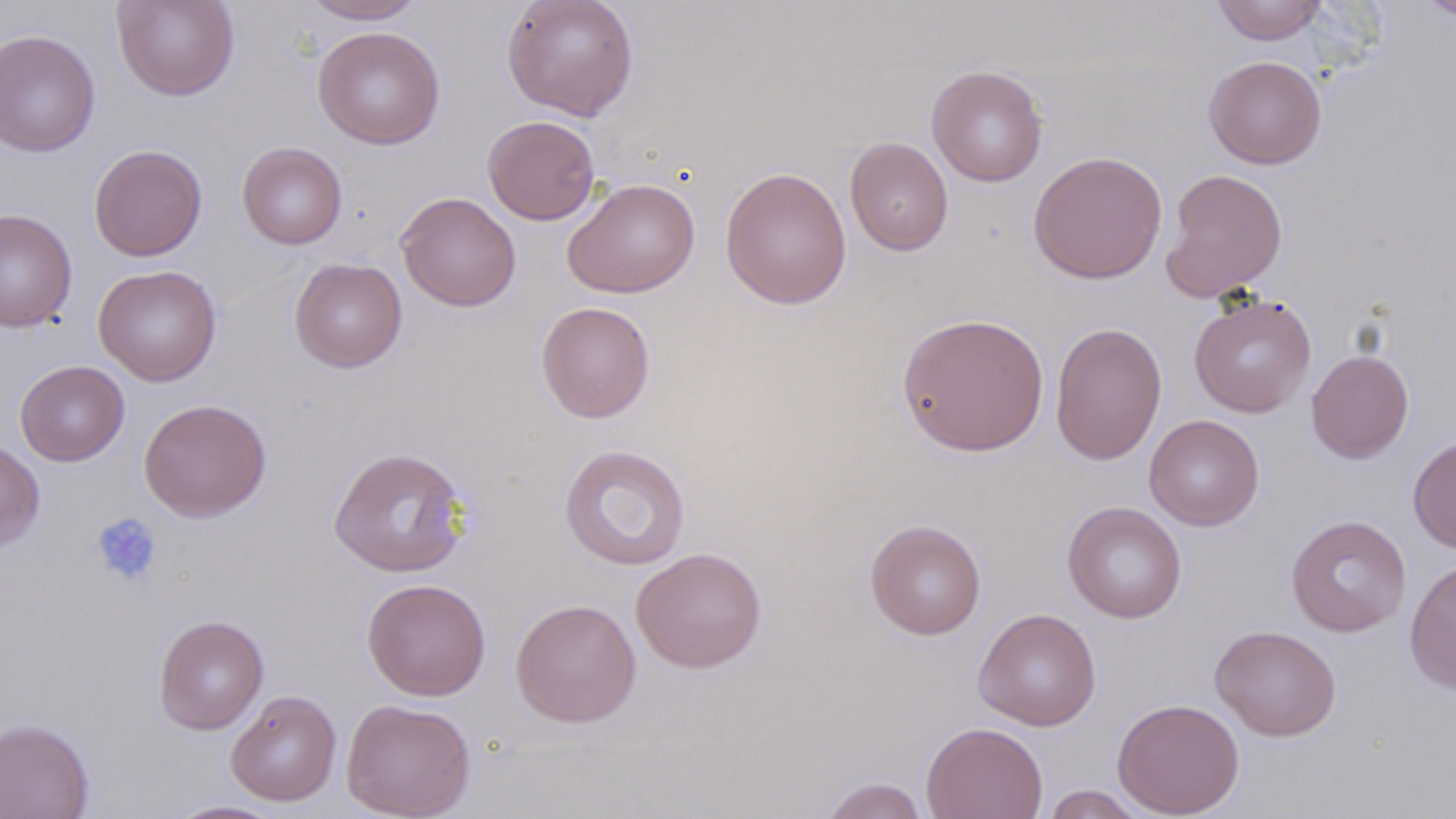

Summary:
  - Coordinate format: approximate bounding boxes as (x1, y1, x2, y2) in pixels
  - Platelet locations: (90, 512, 162, 588)
  - Uninfected red blood cell locations: (111, 0, 240, 101), (300, 0, 427, 24), (502, 0, 639, 121), (1212, 0, 1328, 45), (1418, 0, 1455, 22), (312, 26, 446, 149), (0, 29, 100, 157), (1203, 55, 1327, 169), (927, 65, 1049, 187), (482, 115, 600, 225), (844, 137, 954, 256), (237, 142, 347, 249), (89, 143, 207, 261), (1028, 150, 1168, 285), (720, 166, 852, 310), (1161, 168, 1288, 302), (562, 178, 701, 298), (396, 191, 521, 311), (0, 208, 77, 332), (289, 257, 407, 373), (93, 265, 222, 387), (1189, 293, 1316, 418), (536, 301, 655, 423), (896, 312, 1049, 456), (1049, 321, 1167, 466), (1306, 349, 1414, 464), (15, 360, 130, 466), (138, 398, 272, 522), (1144, 414, 1265, 531), (1408, 435, 1456, 554), (0, 438, 45, 551), (558, 444, 691, 571), (328, 446, 471, 578), (1062, 502, 1187, 623), (1286, 514, 1411, 637), (864, 519, 986, 640), (631, 547, 767, 673), (1404, 556, 1456, 696), (362, 578, 491, 701), (510, 597, 641, 728), (973, 608, 1101, 731), (153, 614, 269, 734), (1209, 625, 1341, 741), (225, 690, 342, 806), (1112, 697, 1245, 817), (340, 698, 476, 819), (0, 717, 95, 818), (921, 721, 1048, 819), (818, 776, 931, 819), (1039, 785, 1149, 818), (163, 799, 291, 819)
  - Slide-level diagnosis: no evidence of blood parasites
  - Modality: light microscopy
  - Magnification: 1000x
  - Stain: May-Grünwald-Giemsa
  - Field of view: one of a larger specimen
  - Preparation: thin blood film
  - Image size: 1456×819 pixels